Classify this cell by malaria status.
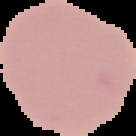
Uninfected.

image_size: 136×136 pixels
image_type: segmented cell region on a black background
preparation: thin blood film